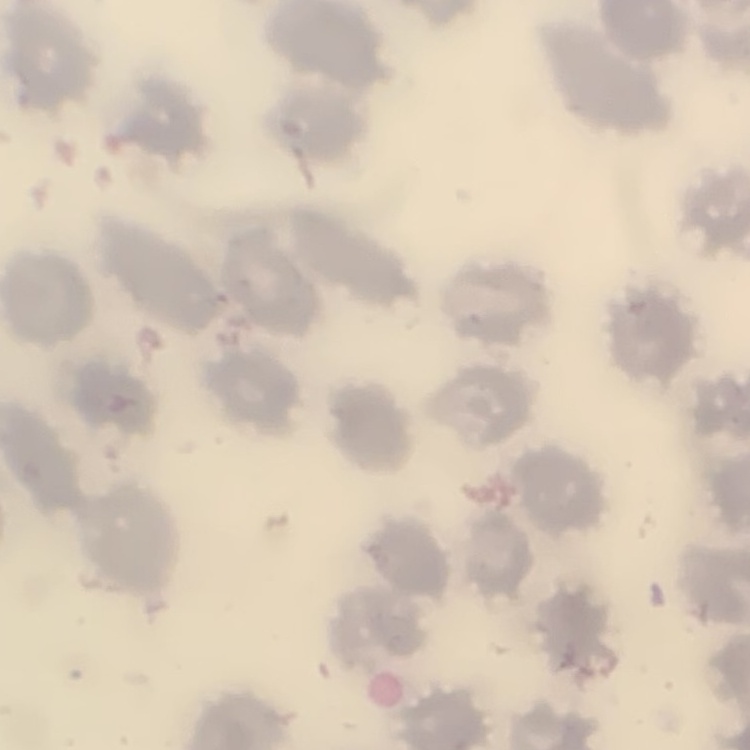

erythrocyte morphology = no rouleaux formation
stain = Field's or Giemsa
preparation = thin blood smear
image type = square crop of a larger photomicrograph